Assess this cell for malaria.
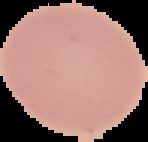

It is uninfected.

Image is 148×142 pixels. From a thin blood film. Cell region segmented out of the field of view; the surrounding area is masked to black.